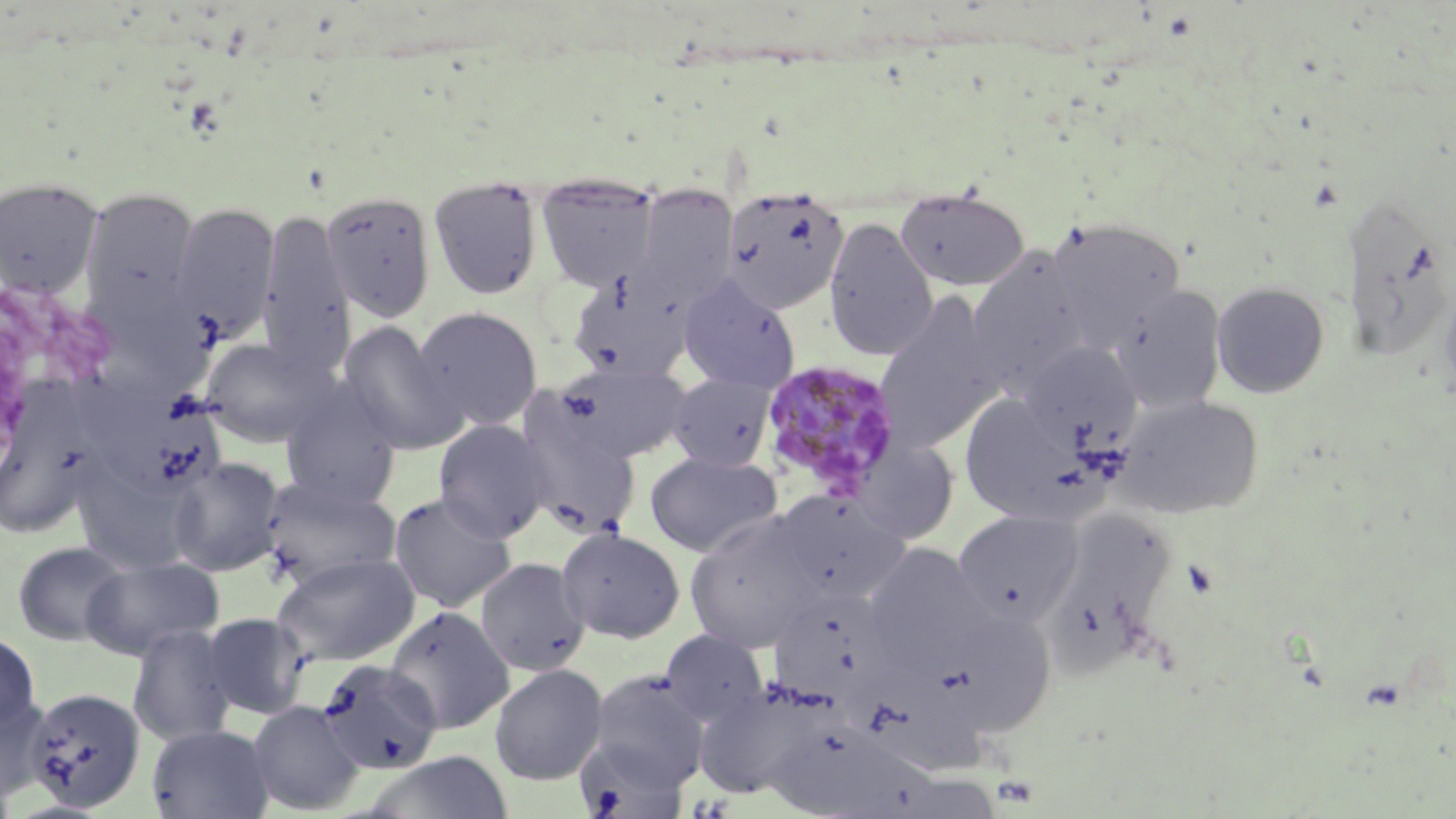

Summary:
  - Coordinate format: approximate bounding boxes as named x1/y1/x2/y2 corners in pixels
  - Uninfected red blood cell locations: (x1=536, y1=175, x2=661, y2=291), (x1=0, y1=176, x2=102, y2=299), (x1=429, y1=176, x2=545, y2=301), (x1=626, y1=186, x2=740, y2=316), (x1=895, y1=187, x2=1030, y2=292), (x1=80, y1=188, x2=200, y2=320), (x1=722, y1=188, x2=849, y2=313), (x1=322, y1=189, x2=437, y2=322), (x1=1345, y1=198, x2=1443, y2=360), (x1=170, y1=202, x2=280, y2=342), (x1=256, y1=209, x2=355, y2=375), (x1=823, y1=217, x2=939, y2=361), (x1=1046, y1=217, x2=1186, y2=347), (x1=967, y1=249, x2=1091, y2=388), (x1=566, y1=267, x2=695, y2=383), (x1=1439, y1=272, x2=1456, y2=400), (x1=678, y1=274, x2=800, y2=391), (x1=1212, y1=281, x2=1330, y2=398), (x1=1112, y1=285, x2=1228, y2=414), (x1=875, y1=294, x2=1004, y2=452), (x1=412, y1=305, x2=544, y2=431), (x1=338, y1=321, x2=468, y2=456), (x1=200, y1=336, x2=331, y2=447), (x1=1019, y1=341, x2=1141, y2=450), (x1=552, y1=362, x2=691, y2=464), (x1=90, y1=371, x2=240, y2=487), (x1=668, y1=373, x2=777, y2=471), (x1=279, y1=381, x2=402, y2=508), (x1=958, y1=394, x2=1094, y2=524), (x1=1117, y1=395, x2=1265, y2=519), (x1=516, y1=412, x2=642, y2=540), (x1=0, y1=416, x2=99, y2=539), (x1=434, y1=419, x2=551, y2=541), (x1=850, y1=438, x2=960, y2=544), (x1=645, y1=451, x2=783, y2=557), (x1=168, y1=456, x2=285, y2=576), (x1=75, y1=467, x2=192, y2=573), (x1=259, y1=475, x2=401, y2=589), (x1=770, y1=490, x2=909, y2=606), (x1=388, y1=491, x2=517, y2=612), (x1=953, y1=509, x2=1082, y2=625), (x1=684, y1=511, x2=823, y2=654), (x1=1048, y1=517, x2=1174, y2=686), (x1=556, y1=526, x2=686, y2=643), (x1=12, y1=540, x2=130, y2=645), (x1=862, y1=543, x2=992, y2=670), (x1=272, y1=553, x2=419, y2=666), (x1=79, y1=555, x2=224, y2=660), (x1=475, y1=557, x2=591, y2=676), (x1=769, y1=585, x2=898, y2=708), (x1=385, y1=605, x2=515, y2=734), (x1=939, y1=605, x2=1058, y2=734), (x1=200, y1=612, x2=312, y2=719), (x1=127, y1=624, x2=238, y2=747), (x1=659, y1=629, x2=770, y2=730), (x1=0, y1=632, x2=41, y2=732), (x1=315, y1=659, x2=444, y2=776), (x1=849, y1=661, x2=991, y2=781), (x1=489, y1=664, x2=608, y2=785), (x1=585, y1=670, x2=710, y2=794), (x1=693, y1=677, x2=833, y2=800), (x1=23, y1=687, x2=147, y2=812), (x1=0, y1=694, x2=52, y2=807), (x1=247, y1=700, x2=365, y2=815), (x1=763, y1=723, x2=940, y2=817), (x1=146, y1=724, x2=275, y2=818), (x1=575, y1=733, x2=689, y2=819), (x1=365, y1=752, x2=515, y2=819)
  - Plasmodium malariae-infected red blood cell locations: (x1=758, y1=359, x2=902, y2=501)
  - Platelet locations: (x1=993, y1=774, x2=1040, y2=809)
  - Slide-level diagnosis: Plasmodium malariae
  - Field of view: single
  - Magnification: 1000x
  - Preparation: thin blood film
  - Image size: 1456×819 pixels
  - Stain: May-Grünwald-Giemsa
  - Modality: optical microscopy